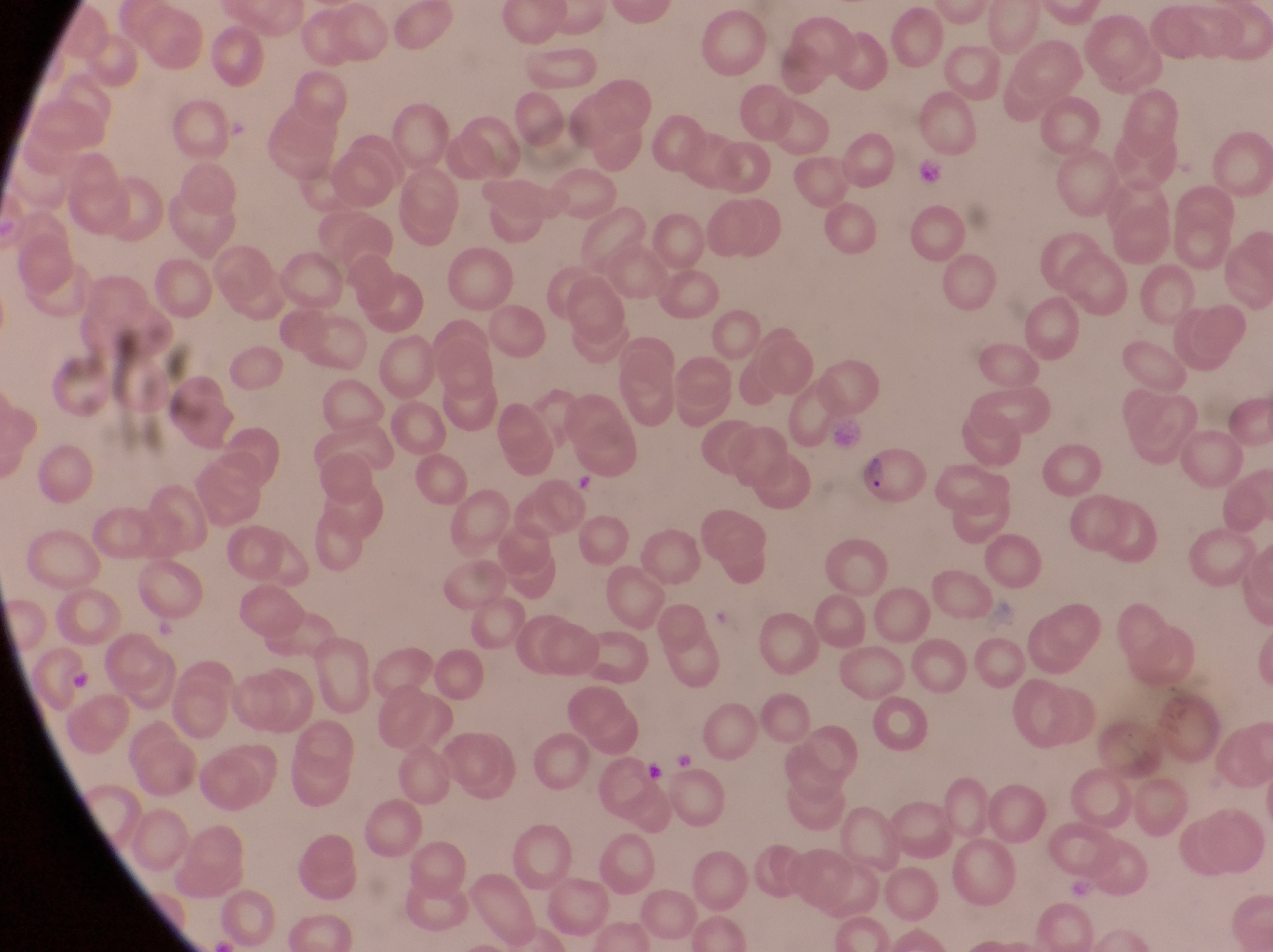
Approximate bounding boxes as left top right bottom in pixels.
Summary:
  - Artifact (platelet-like body, stain precipitate, or debris) locations: 914 151 943 185; 674 746 698 772; 642 759 669 785
  - Parasitised red blood cell locations: 861 445 931 502
  - Magnification: 1000x
  - Field of view: single
  - Capture: smartphone photograph through the eyepiece of an Olympus CX-23 microscope
  - Country: Uganda
  - Preparation: thin blood smear
  - Image size: 1273×952 pixels